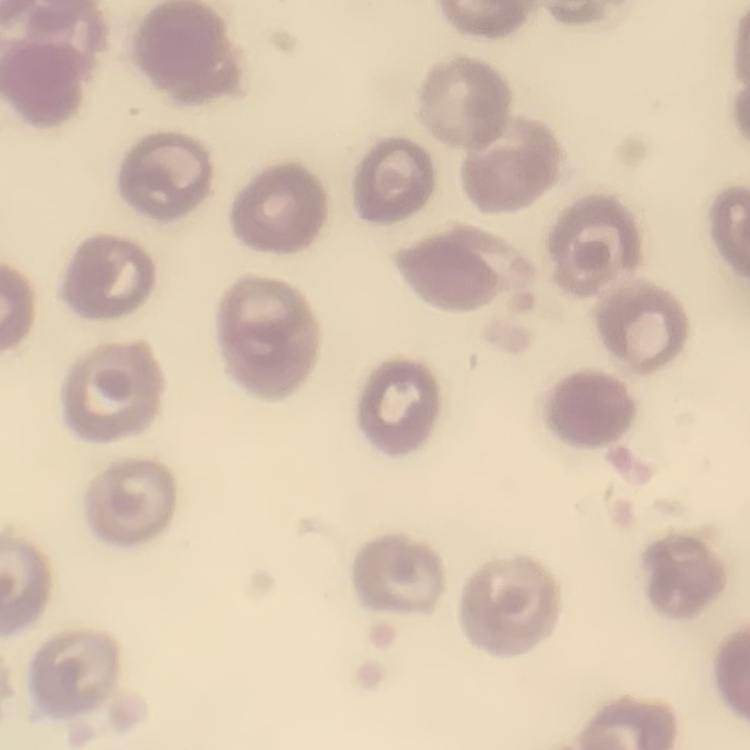

{
  "red_blood_cell_morphology": "no rouleaux formation",
  "stain": "Field's or Giemsa",
  "preparation": "thin blood smear",
  "image_type": "one tile cut from a larger photomicrograph"
}